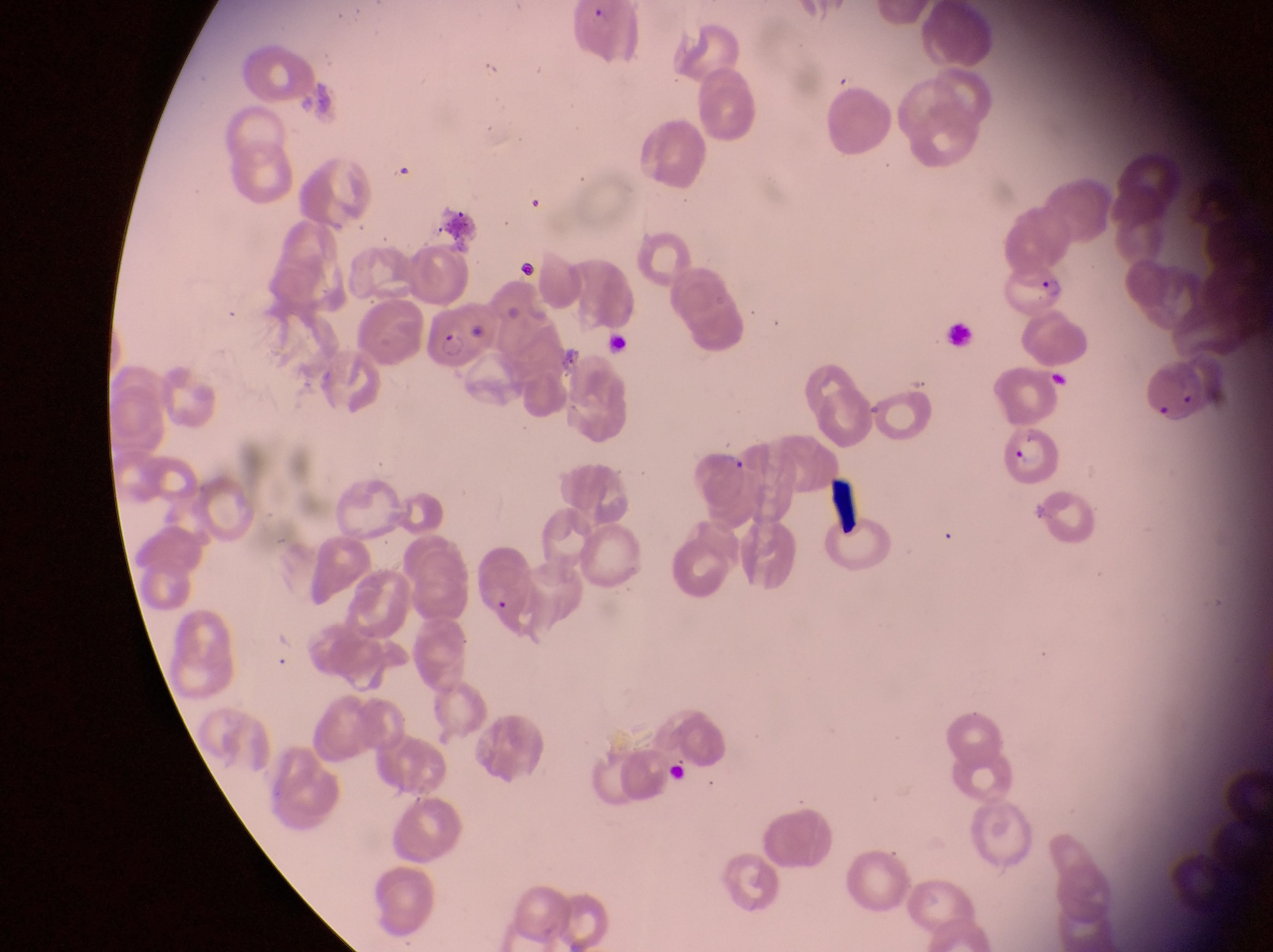
Approximate bounding boxes as {left, top, right, bottom} in pixels.
Summary:
  - Parasitised red blood cell locations: {1001, 259, 1070, 321}, {429, 304, 489, 371}, {1143, 364, 1213, 436}, {1003, 422, 1063, 490}
  - Artifact (platelet-like body, stain precipitate, or debris) locations: {828, 482, 869, 533}
  - Field of view: single
  - Capture: smartphone photograph through the eyepiece of an Olympus CX-23 microscope
  - Preparation: thin blood film
  - Magnification: 1000x
  - Image size: 1273×952 pixels
  - Country: Uganda